Locate the cells, classifying each as a parasitized RBC, an uninfected RBC, or a WBC.
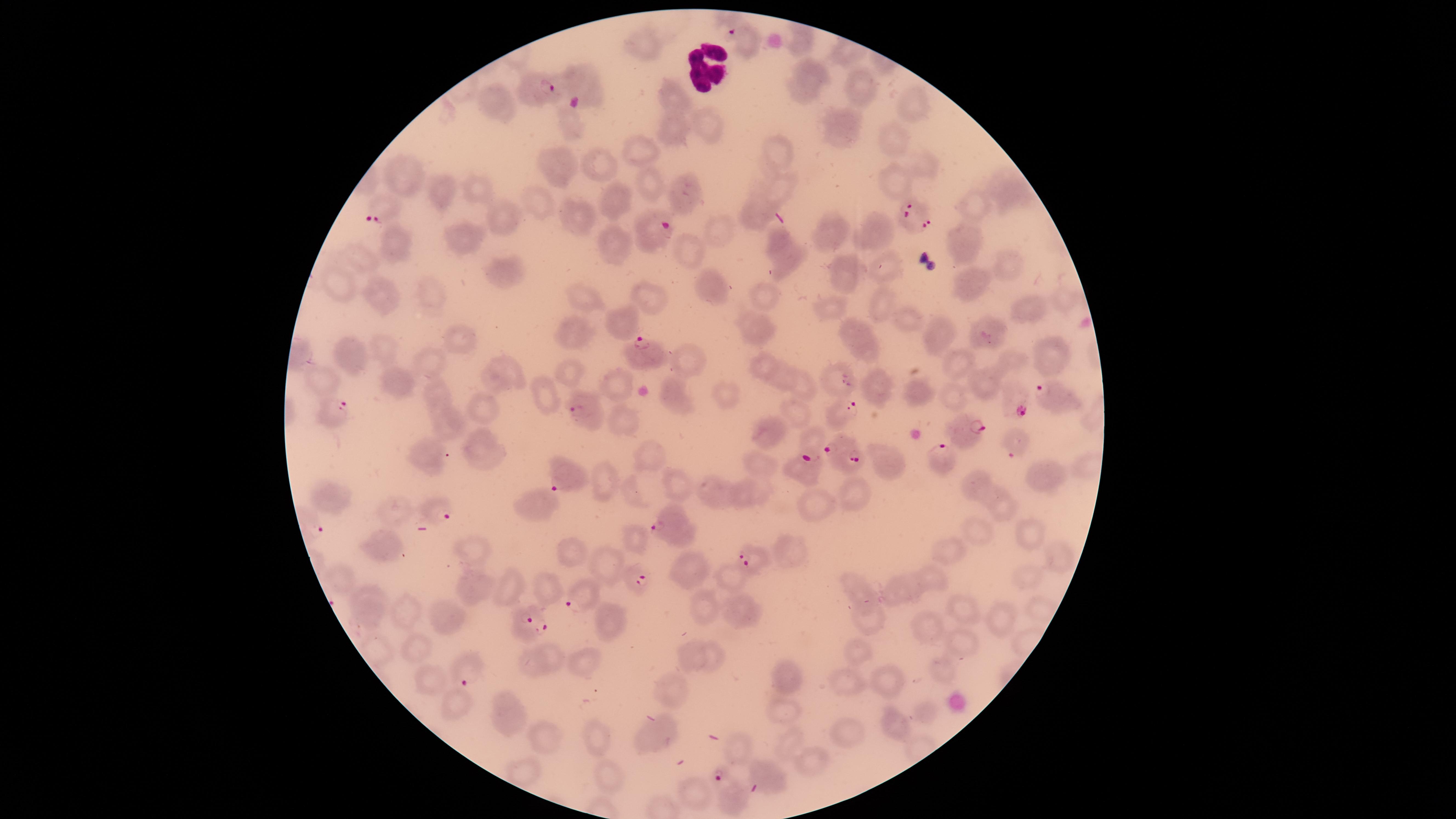
Approximate marker points as [x, y] in pixels.
Parasitized RBCs: [734, 34], [531, 81], [383, 206], [909, 212], [655, 233], [639, 353], [1050, 397], [338, 405], [584, 410], [845, 411], [964, 426], [811, 438], [842, 440], [1013, 443], [854, 462], [939, 463], [563, 475], [432, 508], [662, 515], [746, 559], [639, 580], [577, 598], [524, 624], [468, 676], [719, 776].
Uninfected RBCs: [645, 41], [579, 81], [811, 82], [863, 86], [674, 98], [500, 100], [912, 104], [569, 123], [713, 124], [833, 125], [673, 128], [893, 140], [640, 148], [782, 149], [600, 163], [557, 164], [927, 166], [412, 168], [642, 179], [778, 186], [892, 186], [474, 190], [444, 191], [1008, 192], [682, 198], [614, 199], [534, 201], [972, 202], [754, 218], [577, 220], [873, 223], [502, 224], [717, 228], [836, 232], [455, 237], [962, 239], [606, 241], [399, 245], [688, 245], [787, 252], [357, 255], [1007, 260], [884, 265], [846, 270], [499, 274], [973, 278], [338, 281], [705, 285], [649, 295], [764, 295], [383, 298], [430, 299], [587, 299], [879, 304], [1025, 308], [831, 309], [903, 319], [626, 322], [759, 328], [986, 331], [573, 332], [934, 332], [453, 336], [857, 340], [378, 342], [1044, 353], [354, 354], [959, 361], [429, 362], [694, 363], [1016, 364], [760, 367], [572, 374], [836, 375], [501, 376], [323, 378], [777, 379], [395, 380], [986, 382], [881, 385], [620, 386], [438, 388], [918, 388], [803, 391], [952, 391], [718, 392], [548, 393], [1009, 396], [681, 400], [482, 403], [796, 410], [624, 419], [447, 423], [764, 428], [479, 446], [432, 454], [651, 456], [753, 463], [1047, 473], [605, 480], [678, 482], [978, 485], [712, 490], [631, 491], [852, 491], [747, 493], [328, 497], [812, 500], [540, 501], [1000, 502], [391, 512], [973, 530], [1026, 530], [633, 540], [388, 546], [789, 546], [948, 548], [572, 549], [475, 550], [1061, 558], [605, 559], [685, 564], [1028, 570], [733, 575], [929, 575], [475, 585], [855, 586], [508, 588], [902, 588], [547, 592], [366, 599], [742, 604], [703, 606], [960, 606], [404, 609], [1005, 618], [606, 619], [870, 619], [444, 622], [928, 622], [960, 646], [416, 649], [689, 654], [711, 654], [859, 654], [556, 655], [583, 659], [528, 663], [942, 668], [789, 677], [847, 678], [892, 679], [428, 682], [673, 689], [454, 704], [781, 708], [507, 713], [894, 725], [847, 730], [598, 733], [656, 733], [786, 739], [546, 744], [742, 755], [806, 760], [526, 772], [767, 772], [608, 773], [695, 794], [734, 798].
WBCs: [700, 66].

Photographed with a smartphone camera through the microscope eyepiece. The visible region is circular. Image is 1456×819 pixels. Thin blood film. Species: Plasmodium falciparum. Giemsa-stained preparation. One field of view of the specimen.